Mark where platelets are.
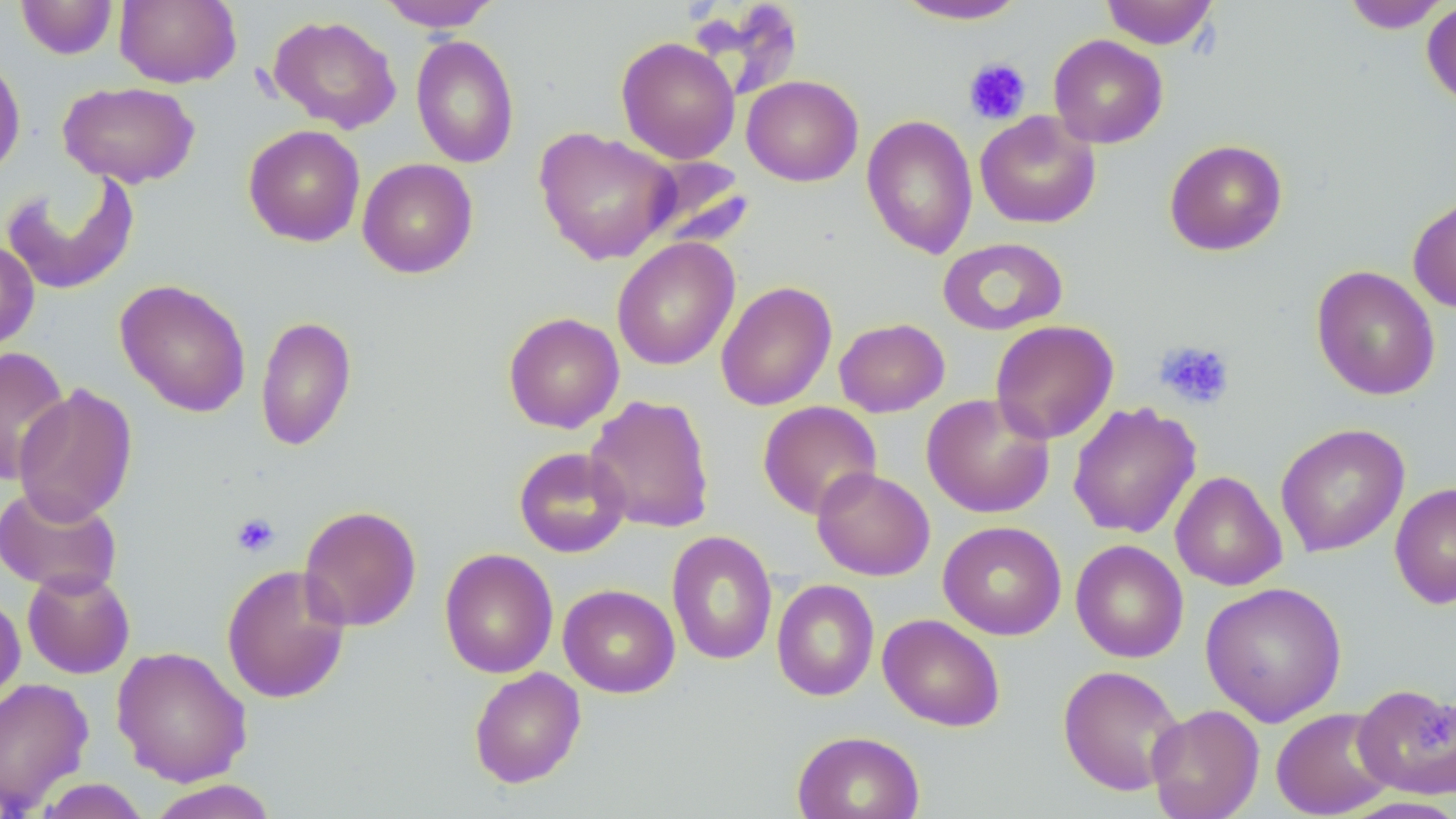

Approximate bounding boxes as [x1, y1, x2, y2] in pixels.
Platelets: [963, 57, 1032, 125], [1155, 340, 1236, 411], [230, 512, 280, 557].

slide-level diagnosis = no evidence of blood parasites
field of view = single
stain = May-Grünwald-Giemsa
uninfected red blood cell locations = approximate bounding boxes as [x1, y1, x2, y2] in pixels: [16, 0, 118, 60], [114, 0, 241, 88], [1099, 0, 1218, 50], [377, 1, 502, 32], [891, 1, 1031, 25], [1340, 1, 1453, 33], [1421, 1, 1456, 110], [267, 14, 402, 133], [410, 34, 520, 169], [1048, 34, 1168, 148], [616, 37, 740, 164], [0, 53, 27, 182], [742, 75, 863, 187], [58, 81, 199, 188], [975, 110, 1101, 229], [859, 114, 1107, 244], [861, 114, 978, 259], [243, 124, 366, 246], [534, 126, 680, 265], [1164, 138, 1288, 256], [637, 157, 755, 253], [357, 158, 478, 278], [1, 170, 141, 296], [1407, 195, 1456, 313], [612, 237, 740, 371], [937, 237, 1068, 336], [0, 240, 39, 353], [1311, 265, 1440, 401], [114, 279, 251, 417], [715, 281, 837, 411], [503, 312, 624, 433], [255, 315, 357, 452], [834, 318, 950, 417], [990, 320, 1119, 443], [1, 345, 70, 486], [13, 383, 138, 525], [921, 393, 1056, 518], [585, 394, 716, 534], [757, 401, 882, 519], [1067, 402, 1201, 539], [1275, 423, 1410, 556], [513, 446, 631, 558], [812, 467, 935, 580], [1170, 470, 1287, 591], [1389, 482, 1456, 610], [0, 485, 123, 596], [298, 504, 422, 632], [938, 520, 1067, 640], [666, 531, 778, 666], [1071, 539, 1189, 663], [440, 548, 558, 679], [221, 563, 351, 704], [21, 568, 135, 679], [771, 579, 879, 701], [1200, 581, 1347, 727], [558, 583, 680, 698], [0, 592, 25, 709], [878, 613, 1005, 731], [111, 645, 252, 786], [1058, 664, 1186, 796], [468, 667, 586, 788], [0, 676, 94, 814], [1353, 684, 1456, 800], [1146, 704, 1264, 819], [1271, 706, 1398, 818], [791, 730, 925, 819], [33, 777, 153, 819], [145, 780, 281, 819], [1336, 795, 1456, 818]
magnification = 1000x
preparation = thin blood smear
image size = 1456×819 pixels
modality = optical microscopy